Assess the morphology of the erythrocytes.
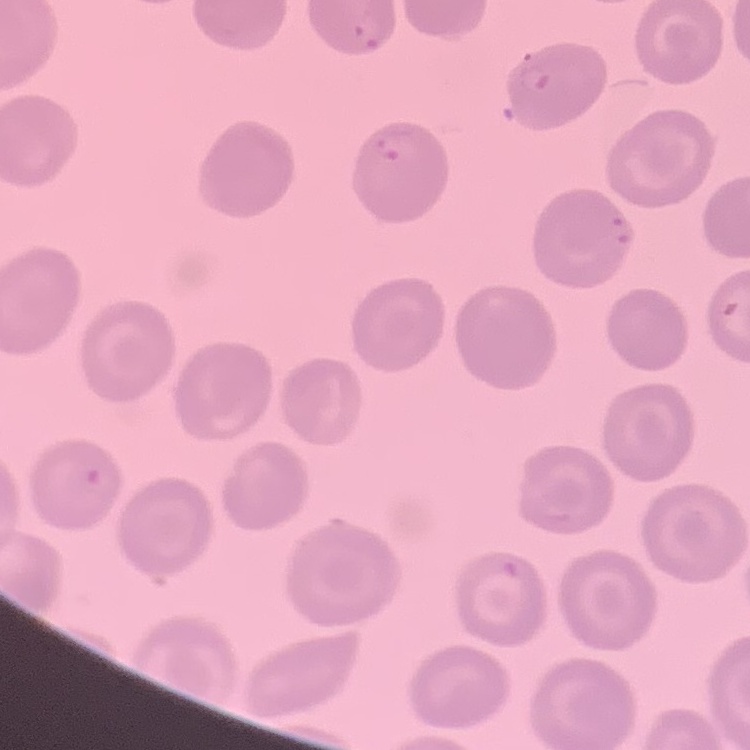

They show no rouleaux formation.

One tile cut from a larger photomicrograph. Field's or Giemsa stain. Thin peripheral smear.